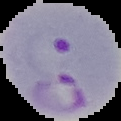

Summary:
  - Result: Plasmodium parasites identified
  - Preparation: thin blood smear
  - Image size: 121×121 pixels
  - Image type: cell region segmented out of the field of view; surrounding area masked to black